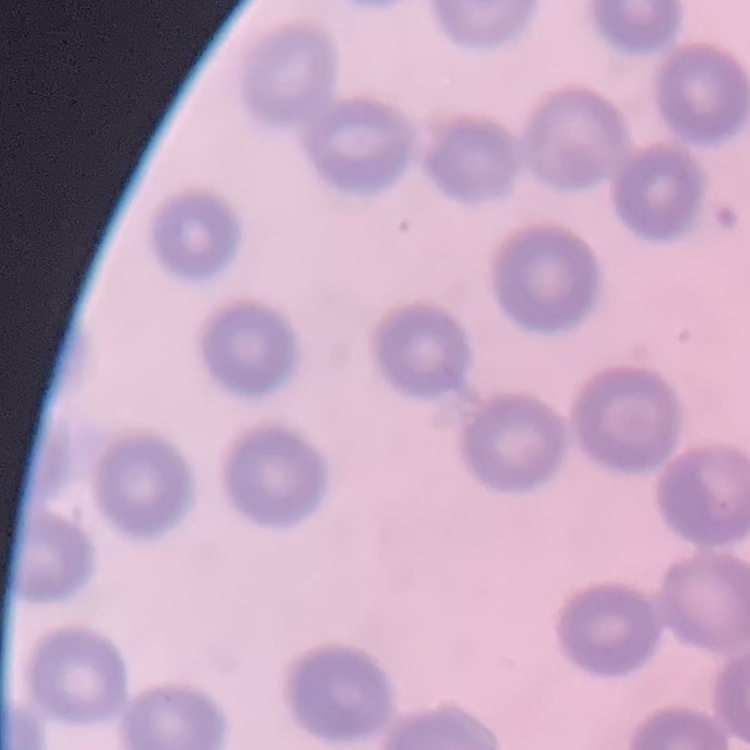
Summary:
  - Red blood cell morphology: no rouleaux formation
  - Image type: square crop of a larger photomicrograph
  - Preparation: thin peripheral smear
  - Stain: Field's or Giemsa